State the blood parasite species.
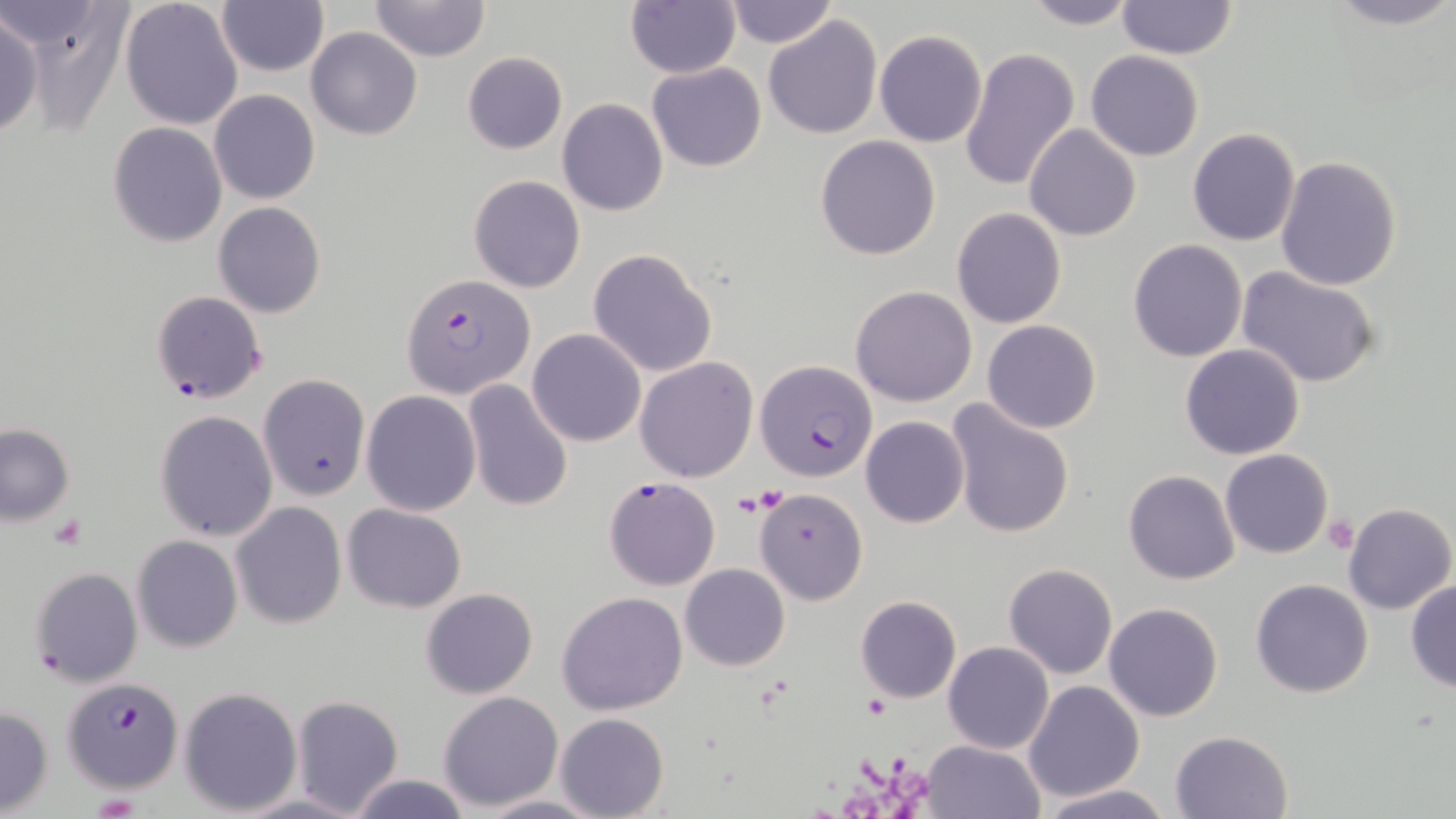

Plasmodium falciparum.

field of view = single
Plasmodium falciparum-infected red blood cell locations = approximate bounding boxes as named x1/y1/x2/y2 corners in pixels: (x1=401, y1=273, x2=535, y2=398), (x1=150, y1=289, x2=266, y2=407), (x1=755, y1=359, x2=877, y2=483), (x1=604, y1=477, x2=720, y2=589), (x1=27, y1=567, x2=143, y2=695), (x1=63, y1=677, x2=183, y2=792)
stain = May-Grünwald-Giemsa
preparation = thin blood smear
modality = optical microscopy
platelet locations = approximate bounding boxes as named x1/y1/x2/y2 corners in pixels: (x1=1325, y1=512, x2=1358, y2=553), (x1=50, y1=513, x2=86, y2=550), (x1=865, y1=694, x2=891, y2=718)
image size = 1456×819 pixels
magnification = 1000x
uninfected red blood cell locations = approximate bounding boxes as named x1/y1/x2/y2 corners in pixels: (x1=14, y1=0, x2=132, y2=135), (x1=216, y1=0, x2=329, y2=76), (x1=370, y1=0, x2=491, y2=63), (x1=625, y1=0, x2=741, y2=79), (x1=725, y1=0, x2=835, y2=48), (x1=1020, y1=0, x2=1140, y2=30), (x1=1320, y1=0, x2=1456, y2=31), (x1=119, y1=1, x2=244, y2=131), (x1=1115, y1=1, x2=1237, y2=61), (x1=0, y1=11, x2=43, y2=139), (x1=763, y1=14, x2=882, y2=140), (x1=306, y1=27, x2=422, y2=141), (x1=874, y1=29, x2=987, y2=147), (x1=959, y1=46, x2=1081, y2=195), (x1=1086, y1=50, x2=1203, y2=161), (x1=462, y1=51, x2=568, y2=154), (x1=647, y1=63, x2=766, y2=172), (x1=209, y1=89, x2=320, y2=204), (x1=557, y1=99, x2=669, y2=218), (x1=107, y1=121, x2=229, y2=248), (x1=1024, y1=123, x2=1143, y2=241), (x1=1188, y1=128, x2=1301, y2=246), (x1=815, y1=135, x2=941, y2=260), (x1=1275, y1=155, x2=1402, y2=291), (x1=468, y1=174, x2=586, y2=293), (x1=213, y1=202, x2=326, y2=318), (x1=952, y1=207, x2=1067, y2=330), (x1=1127, y1=238, x2=1247, y2=362), (x1=587, y1=248, x2=718, y2=378), (x1=1237, y1=266, x2=1385, y2=389), (x1=850, y1=285, x2=978, y2=407), (x1=983, y1=319, x2=1100, y2=434), (x1=528, y1=329, x2=646, y2=446), (x1=1180, y1=344, x2=1305, y2=460), (x1=634, y1=356, x2=758, y2=482), (x1=258, y1=374, x2=371, y2=500), (x1=462, y1=379, x2=574, y2=515), (x1=361, y1=390, x2=482, y2=515), (x1=947, y1=403, x2=1075, y2=540), (x1=154, y1=409, x2=278, y2=542), (x1=860, y1=416, x2=968, y2=528), (x1=0, y1=424, x2=75, y2=524), (x1=1220, y1=449, x2=1333, y2=559), (x1=1123, y1=470, x2=1240, y2=584), (x1=755, y1=488, x2=867, y2=605), (x1=231, y1=501, x2=345, y2=628), (x1=1344, y1=502, x2=1455, y2=615), (x1=343, y1=503, x2=467, y2=613), (x1=127, y1=525, x2=340, y2=644), (x1=132, y1=536, x2=242, y2=654), (x1=680, y1=563, x2=790, y2=671), (x1=1003, y1=563, x2=1118, y2=680), (x1=1250, y1=579, x2=1373, y2=698), (x1=1405, y1=579, x2=1456, y2=692), (x1=421, y1=588, x2=538, y2=698), (x1=557, y1=591, x2=688, y2=716), (x1=854, y1=595, x2=961, y2=703), (x1=1103, y1=602, x2=1224, y2=722), (x1=942, y1=642, x2=1053, y2=753), (x1=1023, y1=680, x2=1145, y2=803), (x1=179, y1=686, x2=303, y2=815), (x1=438, y1=691, x2=564, y2=809), (x1=292, y1=694, x2=403, y2=817), (x1=0, y1=705, x2=53, y2=816), (x1=555, y1=712, x2=669, y2=819), (x1=1170, y1=729, x2=1294, y2=818), (x1=920, y1=739, x2=1047, y2=819), (x1=344, y1=773, x2=475, y2=818), (x1=1036, y1=784, x2=1175, y2=819), (x1=476, y1=794, x2=605, y2=817)